Report the malaria status of this cell.
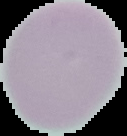

Uninfected.

image type = cell region segmented out of the field of view; surrounding area masked to black
preparation = thin blood smear
image size = 127×136 pixels